State the blood parasite species.
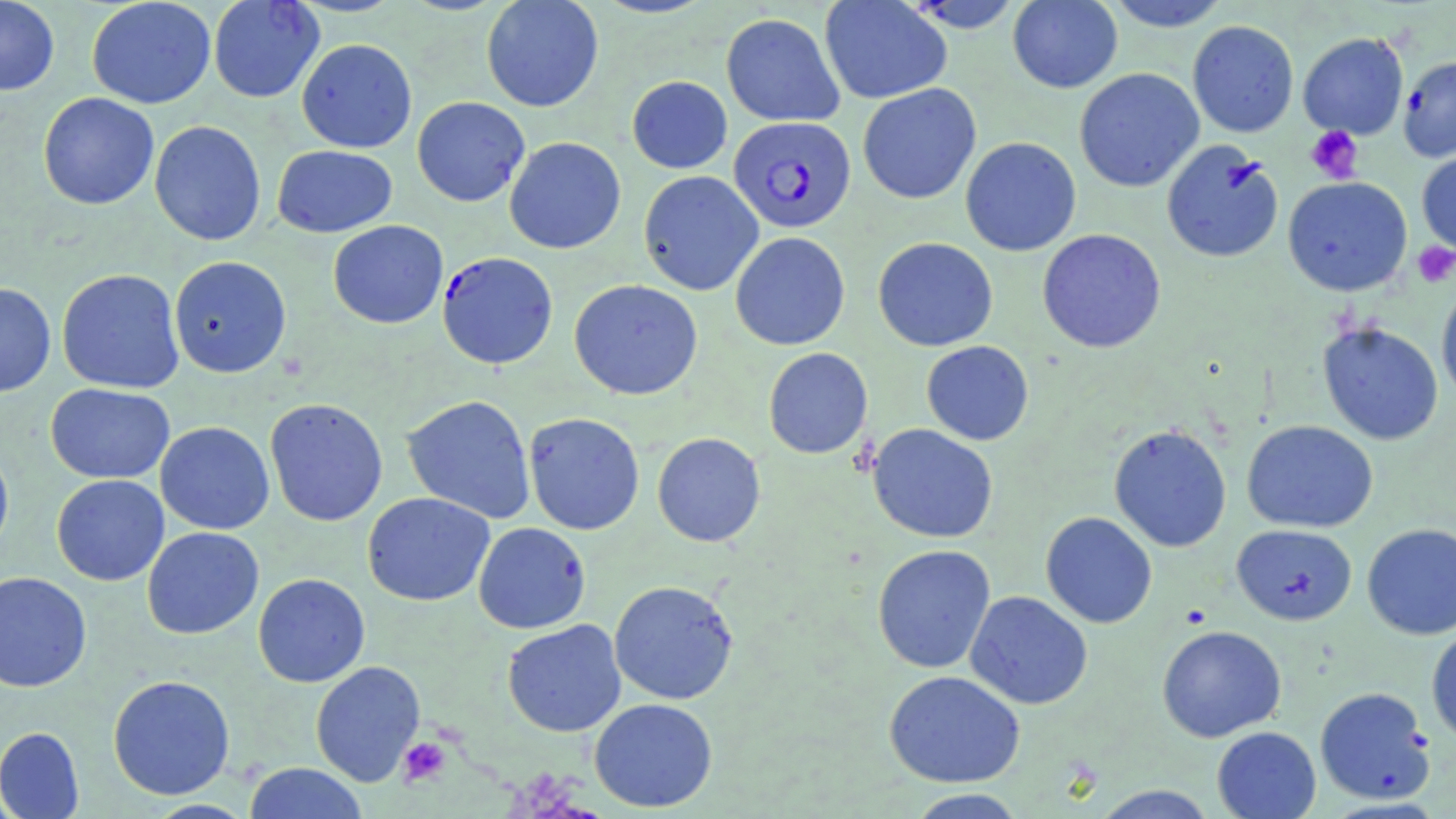

Plasmodium falciparum.

magnification: 1000x
field_of_view: one of a larger specimen
stain: May-Grünwald-Giemsa
uninfected_red_blood_cell_locations: 'approximate bounding boxes as (x1, y1, x2, y2) in pixels: (0, 0, 60, 96), (86, 0, 216, 109), (208, 0, 325, 103), (481, 0, 604, 112), (819, 0, 952, 104), (901, 0, 1026, 33), (1007, 0, 1122, 93), (1102, 0, 1231, 31), (720, 12, 845, 126), (1187, 20, 1299, 138), (1298, 32, 1409, 139), (296, 38, 417, 153), (1398, 55, 1456, 162), (1074, 67, 1204, 192), (627, 75, 732, 173), (857, 83, 981, 205), (38, 92, 159, 210), (411, 96, 530, 206), (149, 120, 266, 246), (504, 136, 626, 254), (960, 137, 1082, 256), (1160, 140, 1284, 264), (272, 145, 397, 237), (1416, 150, 1456, 256), (638, 171, 763, 296), (1283, 176, 1413, 296), (328, 220, 448, 329), (1037, 229, 1166, 353), (730, 232, 850, 351), (873, 237, 998, 352), (169, 256, 291, 378), (56, 269, 185, 394), (569, 279, 703, 400), (1436, 281, 1456, 405), (0, 282, 57, 397), (1317, 321, 1444, 445), (921, 340, 1034, 445), (763, 347, 872, 459), (45, 383, 175, 484), (401, 394, 537, 524), (265, 398, 388, 526), (523, 412, 645, 535), (1241, 420, 1378, 533), (155, 421, 274, 534), (867, 424, 998, 543), (1108, 424, 1232, 552), (652, 432, 766, 547), (0, 440, 14, 564), (51, 474, 169, 586), (362, 492, 495, 606), (1041, 511, 1157, 629), (473, 521, 590, 634), (1362, 523, 1456, 639), (1231, 524, 1357, 625), (141, 527, 264, 639), (872, 544, 996, 674), (0, 571, 92, 692), (253, 573, 370, 687), (609, 580, 739, 705), (965, 591, 1093, 710), (502, 619, 626, 738), (1156, 625, 1287, 743), (1426, 626, 1456, 745), (310, 660, 426, 786), (883, 670, 1025, 788), (107, 674, 235, 800), (1314, 686, 1435, 805), (589, 698, 718, 812), (1211, 726, 1321, 819), (0, 727, 84, 819), (243, 763, 368, 819), (1090, 784, 1219, 818), (906, 788, 1027, 818)'
preparation: thin blood smear
image_size: 1456×819 pixels
platelet_locations: 'approximate bounding boxes as (x1, y1, x2, y2) in pixels: (1305, 126, 1364, 184), (1412, 242, 1456, 288), (1180, 603, 1212, 629), (398, 737, 452, 787)'
plasmodium_falciparum_infected_red_blood_cell_locations: 'approximate bounding boxes as (x1, y1, x2, y2) in pixels: (729, 116, 856, 232), (437, 251, 558, 370)'
modality: light microscopy